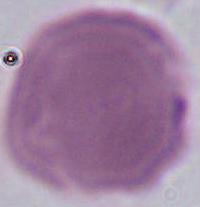 Micrograph. 1000x magnification. A red blood cell is shown.